Identify the cell.
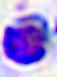
A leukocyte.

400x magnification. Micrograph.